Point out each Plasmodium parasite.
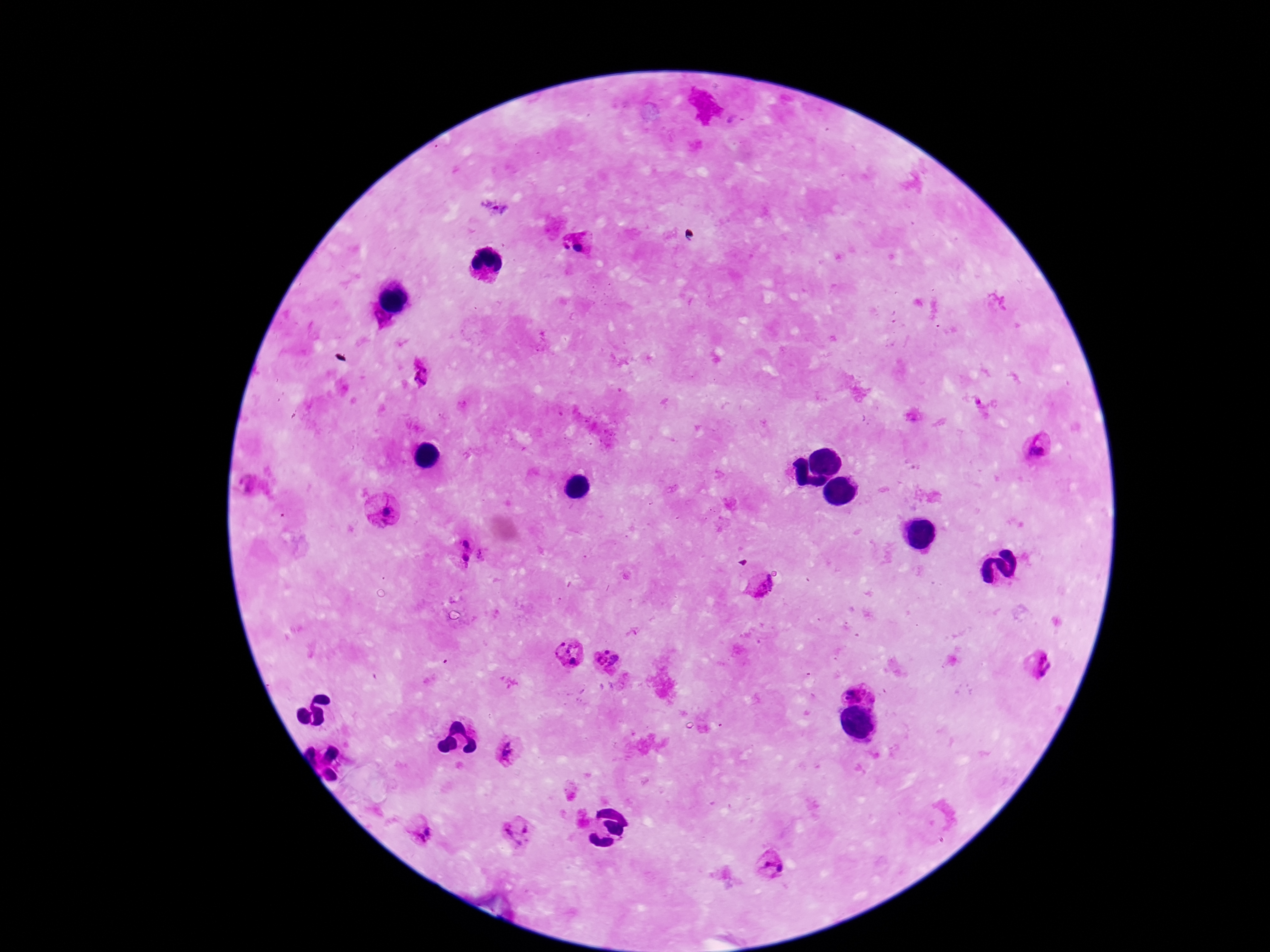
Approximate centers as {x, y} in pixels.
Plasmodium parasites: {579, 242}, {421, 372}, {1038, 448}, {384, 512}, {466, 539}, {465, 562}, {761, 587}, {569, 653}, {609, 659}, {1036, 663}, {858, 690}, {512, 751}, {421, 830}, {518, 835}, {771, 864}.

Summary:
  - Magnification: 100x
  - Preparation: thick blood film
  - Capture: smartphone camera through the microscope eyepiece
  - Patient malaria status: positive
  - Image size: 1270×952 pixels
  - Stain: Giemsa
  - Field of view: single